Locate every leukocyte (white blood cell).
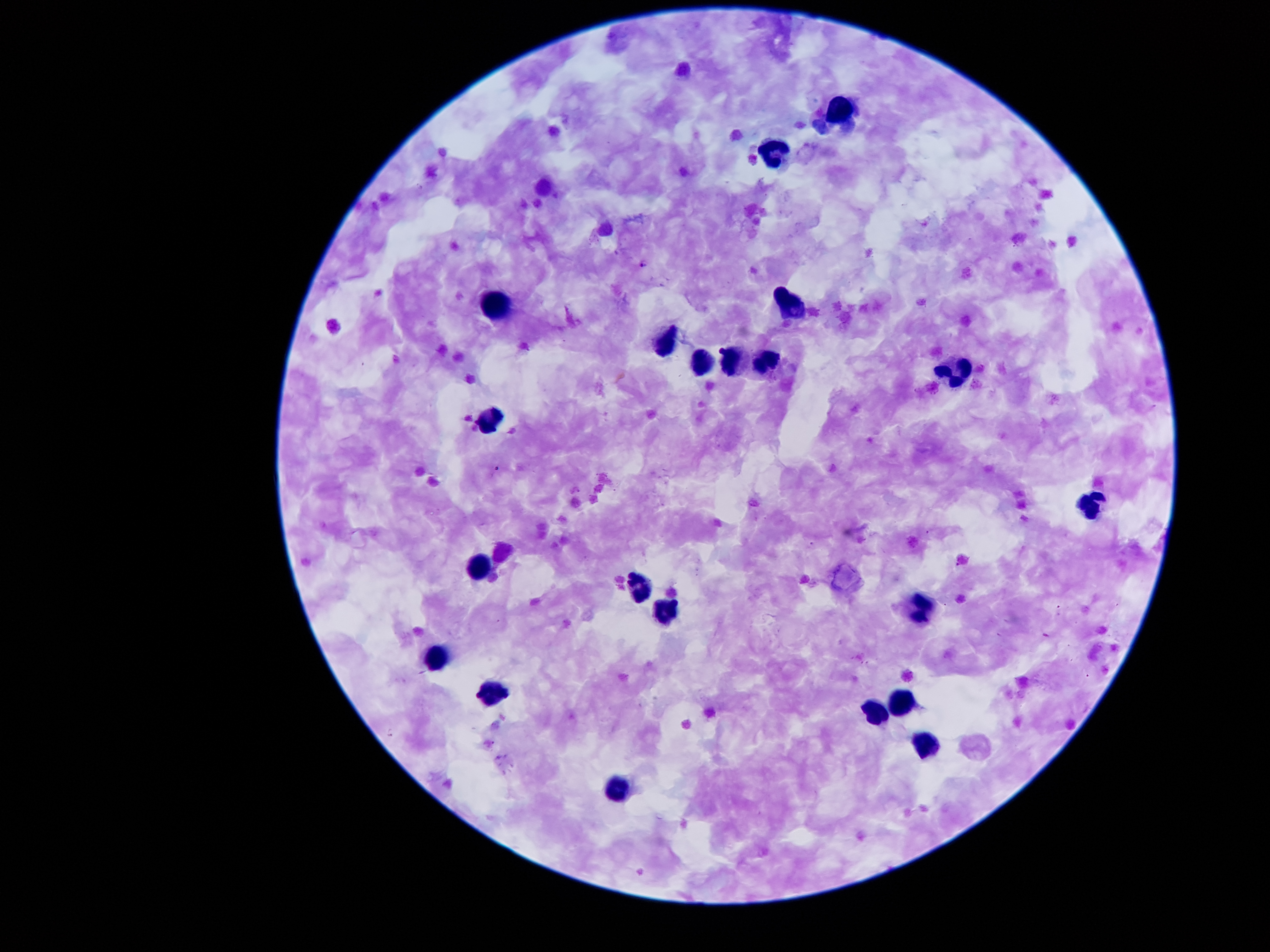
Approximate centers as (x, y) in pixels.
Leukocytes: (839, 106), (770, 150), (785, 297), (496, 300), (670, 337), (729, 357), (702, 360), (760, 362), (956, 373), (493, 420), (1091, 505), (478, 568), (641, 584), (922, 603), (664, 611), (437, 658), (493, 695), (901, 700), (874, 714), (926, 743), (618, 790).

malaria parasite locations = (643, 261), (495, 470), (927, 534), (812, 543), (957, 566), (1060, 608), (391, 732)
preparation = thick peripheral-blood smear
patient malaria status = positive for Plasmodium falciparum
field of view = one from this slide
image size = 1270×952 pixels
capture = smartphone through the microscope eyepiece
magnification = 100x
stain = Giemsa